Locate every parasitized red blood cell.
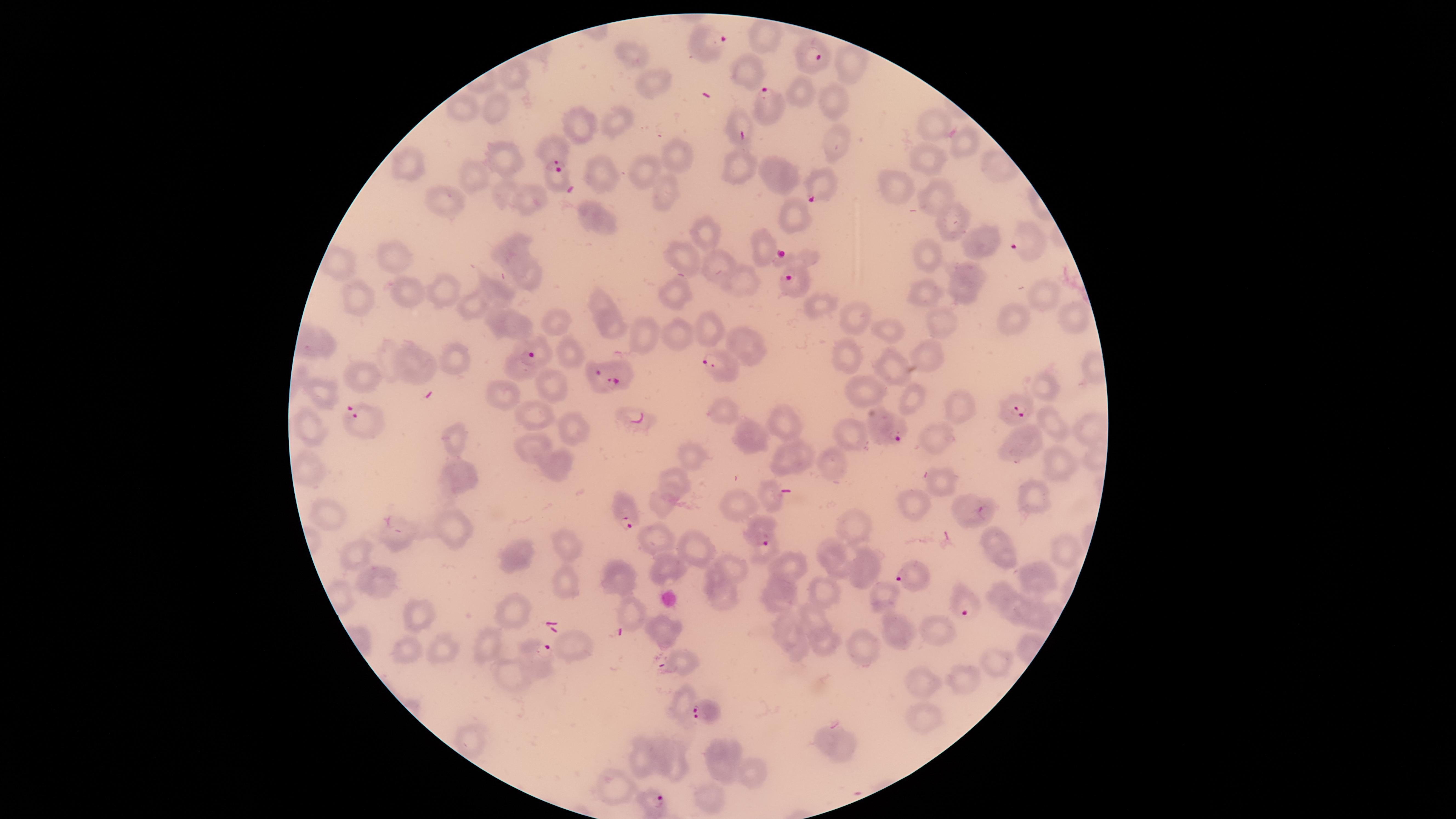

Approximate marker points as [x, y] in pixels.
Parasitized red blood cells: [709, 39], [818, 61], [765, 92], [559, 177], [825, 188], [1020, 243], [790, 276], [536, 350], [719, 365], [607, 377], [1021, 411], [359, 414], [639, 417], [891, 431], [624, 515], [763, 531], [911, 576], [960, 602], [536, 656], [705, 713], [653, 799].

Approximate marker points as [x, y] in pixels. Uninfected red blood cells: [761, 35], [630, 55], [752, 67], [853, 67], [520, 75], [651, 79], [801, 92], [833, 96], [465, 104], [498, 104], [619, 119], [739, 119], [579, 122], [934, 123], [838, 143], [963, 144], [561, 147], [675, 152], [506, 157], [416, 161], [930, 162], [740, 164], [642, 170], [603, 172], [775, 172], [478, 173], [900, 182], [932, 192], [671, 194], [445, 196], [505, 196], [526, 201], [948, 213], [792, 215], [604, 219], [710, 233], [977, 243], [764, 246], [512, 252], [396, 253], [685, 254], [926, 254], [797, 256], [338, 262], [718, 265], [966, 276], [746, 277], [530, 280], [449, 285], [360, 288], [1042, 291], [408, 292], [924, 292], [673, 293], [502, 294], [472, 302], [603, 303], [819, 307], [1071, 313], [857, 315], [1012, 315], [942, 322], [513, 323], [613, 324], [558, 325], [712, 326], [893, 326], [312, 337], [680, 337], [645, 339], [747, 341], [841, 353], [924, 353], [571, 356], [460, 358], [416, 364], [892, 364], [523, 371], [358, 379], [553, 380], [1048, 384], [324, 386], [869, 387], [504, 388], [913, 403], [960, 405], [722, 409], [538, 416], [784, 422], [1052, 423], [1085, 424], [315, 425], [573, 428], [452, 433], [851, 433], [939, 435], [751, 438], [1023, 439], [531, 442], [804, 447], [692, 458], [1058, 461], [558, 462], [829, 462], [785, 464], [313, 469], [458, 472], [675, 478], [941, 481], [770, 494], [733, 502], [914, 505], [1032, 505], [662, 507], [967, 509], [334, 513], [860, 526], [396, 533], [455, 533], [647, 535], [564, 540], [995, 541], [1055, 547], [695, 548], [510, 550], [356, 551], [763, 553], [1004, 557], [834, 559], [792, 564], [862, 564], [666, 568], [731, 572], [620, 577], [376, 579], [564, 580], [1042, 580], [777, 590], [822, 590], [718, 593], [886, 595], [1000, 595], [631, 612], [1010, 612], [1035, 612], [515, 615], [422, 616], [811, 616], [788, 627], [938, 631], [666, 632], [897, 633], [488, 644], [829, 644], [409, 645], [440, 646], [576, 646], [864, 647], [800, 652], [997, 660], [680, 663], [512, 677], [964, 678], [921, 683], [679, 702], [924, 714], [833, 743], [641, 757], [660, 758], [724, 761], [676, 764], [750, 773], [613, 785], [710, 796]. Species: Plasmodium falciparum. One field of view of the specimen. The visible region is circular. Thin smear of blood. Giemsa stain. Image is 1456×819 pixels. Photographed with a smartphone camera through the microscope eyepiece.